Report the malaria status.
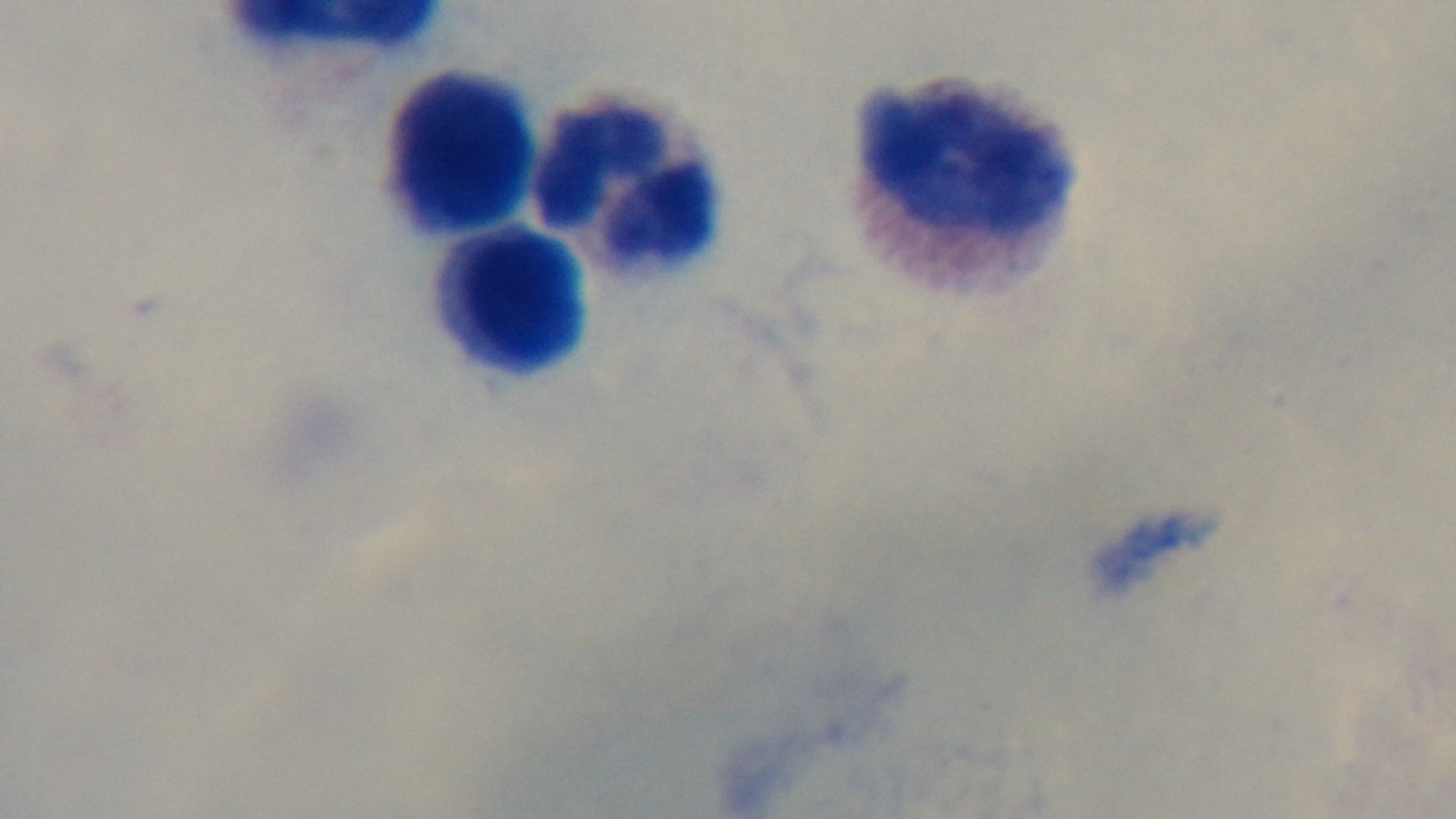
It is uninfected.

Giemsa-stained. One field from the slide. 100x oil-immersion objective. Light microscopy. Mounted 4K digital camera. Preparation: thick smear.